Report the malaria status of this cell.
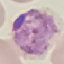
It is parasitized.

Automatically extracted cell patch, resized to 64 × 64 pixels. Thin blood film. Giemsa-stained preparation. Acquired by smartphone through the microscope eyepiece.